Assess this cell for malaria.
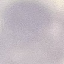

It is uninfected.

Giemsa-stained preparation. Cell patch, automatically extracted from a larger field of view and resized to 64 × 64 pixels. Thin smear of blood. Acquired by smartphone through the microscope eyepiece.